Identify the parasite.
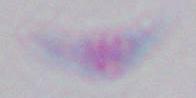

This is Toxoplasma gondii.

magnification = 1000x
modality = photomicrograph